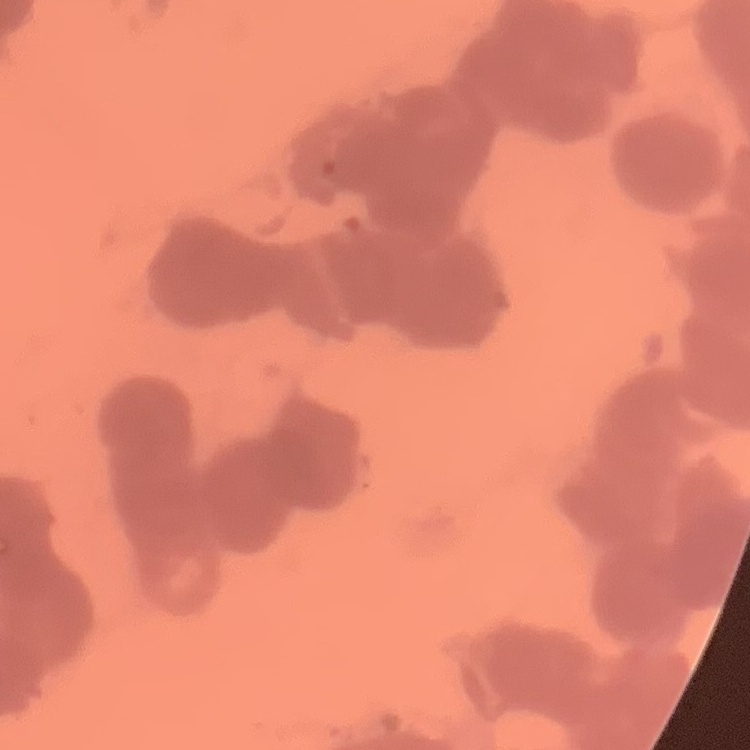

The erythrocytes exhibit rouleaux formation. Stained with either Field's or Giemsa. Thin blood film. One tile cut from a larger photomicrograph.